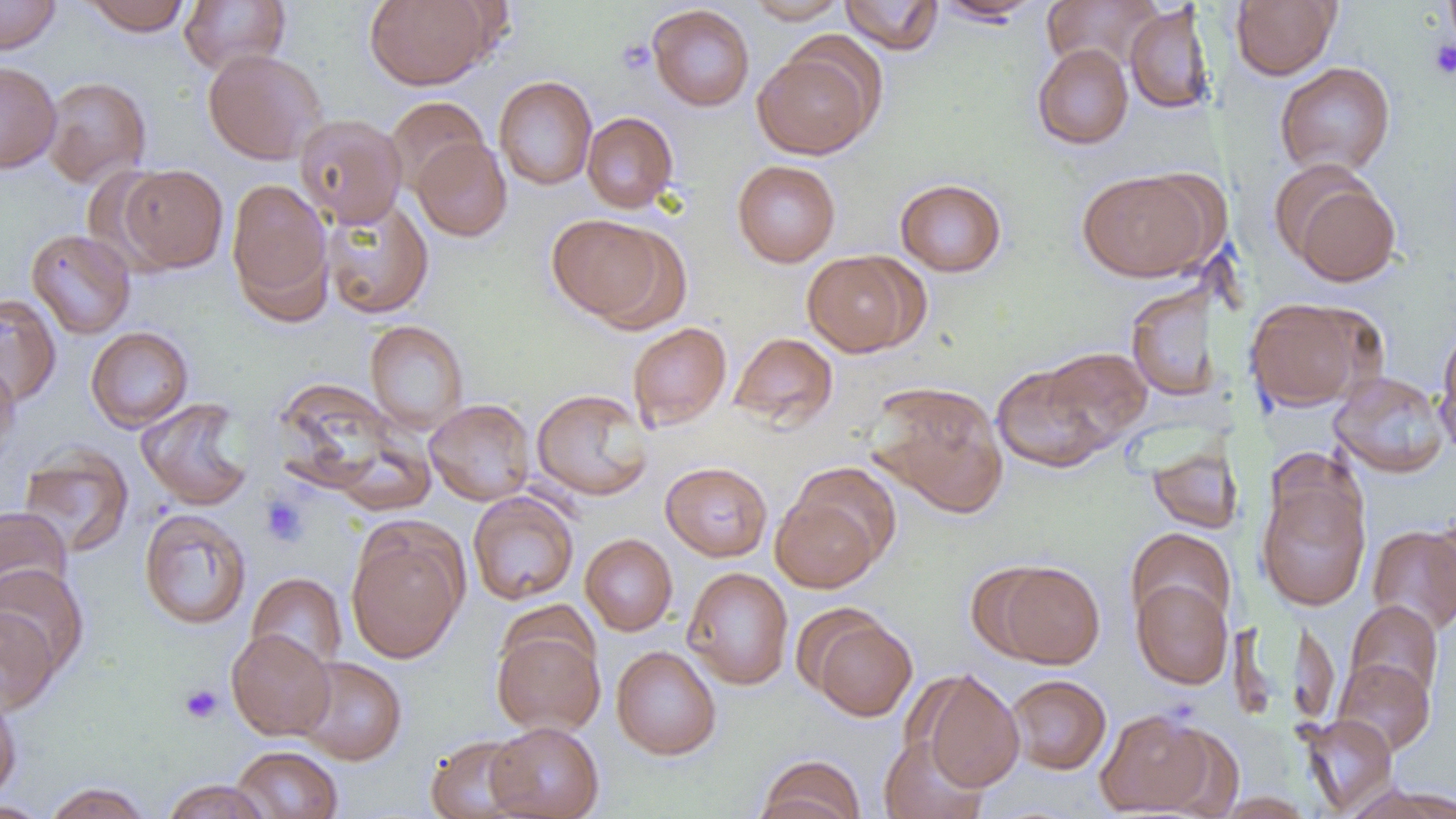

Summary:
  - Coordinate format: approximate bounding boxes as (x1,y1)-(x2,y2) corner pairs in pixels
  - Platelet locations: (617,38)-(655,75), (1428,39)-(1456,80), (259,494)-(309,548), (179,683)-(223,724)
  - Uninfected red blood cell locations: (0,0)-(61,55), (82,0)-(191,36), (364,0)-(496,90), (743,0)-(848,24), (839,0)-(943,55), (933,0)-(1043,24), (1043,0)-(1162,74), (1229,0)-(1341,80), (179,1)-(291,75), (647,4)-(755,111), (1125,4)-(1215,115), (1032,43)-(1133,149), (753,45)-(881,160), (203,49)-(327,165), (0,61)-(61,174), (1274,61)-(1396,177), (41,76)-(151,188), (494,76)-(597,190), (385,96)-(489,193), (582,112)-(678,213), (294,113)-(407,227), (411,137)-(512,242), (732,160)-(841,267), (81,163)-(177,274), (118,164)-(228,273), (1279,167)-(1402,288), (1077,169)-(1216,282), (226,178)-(333,315), (895,178)-(1007,277), (321,196)-(434,320), (547,214)-(672,326), (26,229)-(136,339), (802,250)-(922,357), (1125,282)-(1222,403), (1,293)-(61,408), (1244,297)-(1379,412), (365,320)-(468,434), (627,322)-(732,431), (86,326)-(193,432), (1435,326)-(1456,457), (729,332)-(839,430), (1030,347)-(1151,453), (0,359)-(20,462), (990,360)-(1121,474), (1329,371)-(1450,478), (271,377)-(415,503), (867,382)-(1009,518), (531,389)-(653,501), (136,398)-(254,510), (425,399)-(536,505), (1146,442)-(1243,534), (19,444)-(134,558), (661,461)-(773,562), (1256,478)-(1370,611), (771,487)-(885,593), (468,491)-(579,605), (0,506)-(72,608), (139,508)-(252,630), (1426,509)-(1456,620), (346,522)-(468,664), (1367,525)-(1456,635), (1125,528)-(1236,630), (580,533)-(677,636), (986,560)-(1106,669), (0,564)-(89,676), (682,566)-(794,690), (246,573)-(347,674), (1131,579)-(1233,689), (1345,600)-(1444,703), (0,607)-(60,714), (806,612)-(917,721), (492,628)-(605,736), (226,629)-(335,740), (611,645)-(721,760), (294,656)-(407,765), (1333,657)-(1435,756), (914,669)-(1025,793), (1007,674)-(1111,774), (0,688)-(22,804), (1096,708)-(1216,817), (1300,714)-(1397,815), (486,721)-(604,819), (1155,723)-(1245,818), (425,734)-(533,819), (878,734)-(988,819), (231,745)-(344,818), (753,755)-(866,819), (161,779)-(272,819), (42,782)-(153,819), (1345,782)-(1456,819), (1214,792)-(1314,818), (1,800)-(52,819)
  - Slide-level diagnosis: no evidence of blood parasites
  - Magnification: 1000x
  - Preparation: thin blood smear
  - Image size: 1456×819 pixels
  - Modality: optical microscopy
  - Field of view: single